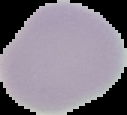
image_type: cell region segmented out of the field of view; surrounding area masked to black
result: negative for Plasmodium parasites
image_size: 127×115 pixels
preparation: thin blood film